Comment on the morphology of the red blood cells.
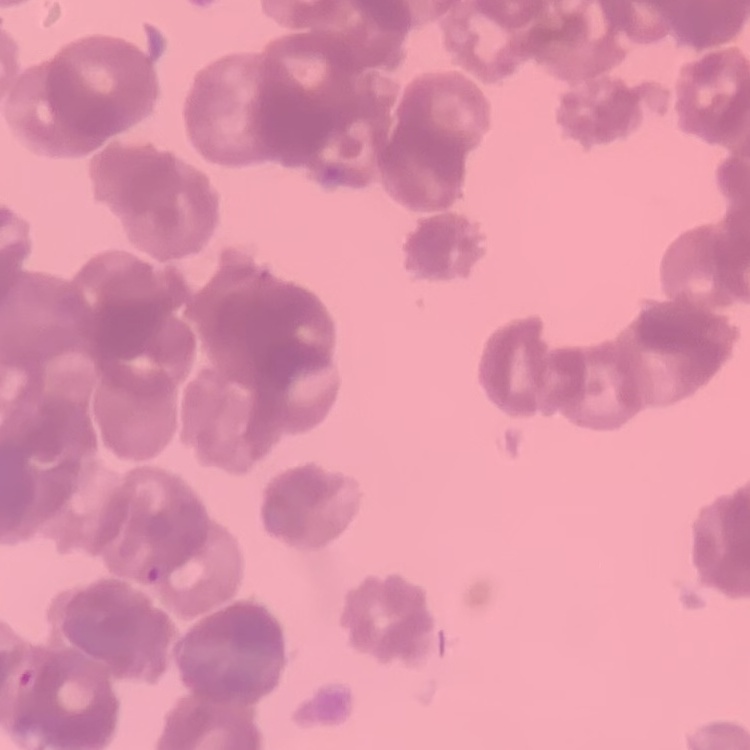
They show rouleaux formation.

One tile cut from a larger photomicrograph. Thin peripheral smear. Stained with either Field's or Giemsa.